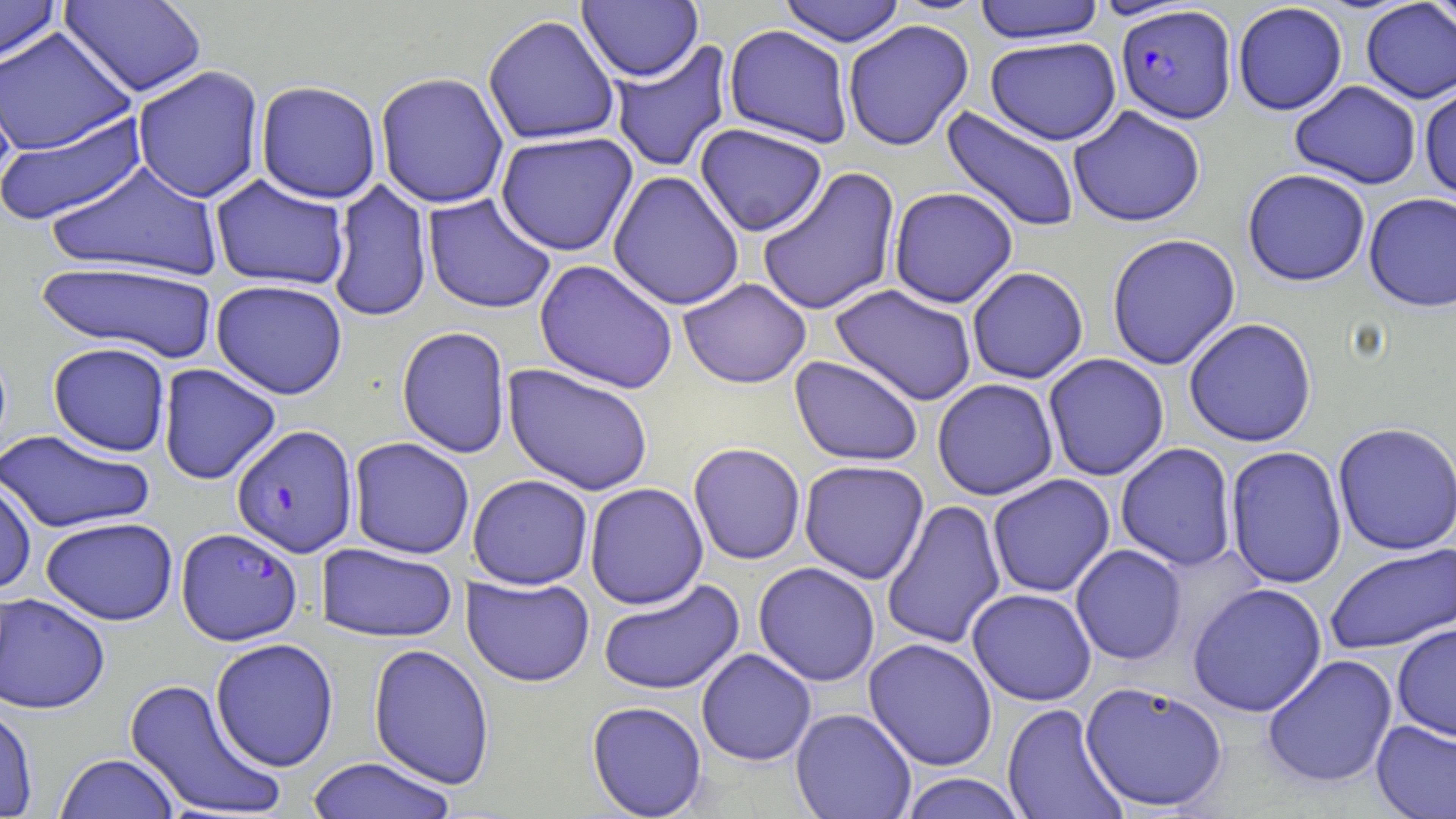

Approximate bounding boxes as (x1,y1)-(x2,y2) corner pairs in pixels. Uninfected red blood cell locations: (0,0)-(63,67), (59,0)-(207,98), (1425,0)-(1455,34), (577,1)-(703,82), (779,1)-(906,47), (973,1)-(1107,44), (1232,2)-(1348,116), (1359,2)-(1456,104), (482,13)-(620,146), (842,19)-(973,151), (723,24)-(855,148), (0,26)-(136,156), (985,36)-(1122,145), (609,39)-(734,173), (0,56)-(19,196), (131,65)-(265,203), (374,71)-(510,209), (254,80)-(382,204), (1289,80)-(1422,189), (1418,84)-(1456,201), (1068,105)-(1206,227), (940,106)-(1081,235), (0,110)-(148,226), (694,123)-(828,237), (494,131)-(638,257), (45,160)-(224,282), (757,166)-(901,317), (1242,168)-(1371,287), (607,170)-(745,311), (209,174)-(351,291), (327,179)-(433,323), (888,187)-(1019,308), (1363,192)-(1456,312), (422,194)-(557,315), (1105,233)-(1241,370), (534,259)-(679,394), (35,260)-(220,361), (966,266)-(1089,384), (678,277)-(812,389), (210,279)-(348,399), (830,284)-(978,406), (1183,317)-(1318,447), (396,325)-(512,459), (47,341)-(172,456), (1043,353)-(1170,481), (789,356)-(924,467), (157,364)-(281,485), (502,364)-(654,496), (932,378)-(1058,500), (1332,422)-(1456,555), (0,429)-(155,534), (348,437)-(475,559), (688,442)-(806,565), (1115,442)-(1238,571), (1225,446)-(1347,589), (798,460)-(929,584), (467,474)-(593,590), (987,474)-(1115,598), (0,476)-(37,596), (584,483)-(709,609), (880,499)-(1006,650), (41,516)-(178,626), (316,542)-(458,643), (1324,543)-(1456,654), (1070,544)-(1187,665), (753,562)-(880,686), (461,575)-(595,687), (597,579)-(745,696), (1186,583)-(1327,717), (967,588)-(1097,706), (0,592)-(111,714), (1392,622)-(1456,741), (863,637)-(998,771), (210,638)-(339,772), (368,643)-(496,790), (696,648)-(817,766), (1262,654)-(1398,789), (124,677)-(287,818), (1079,680)-(1228,813), (586,700)-(708,818), (0,703)-(38,819), (1001,703)-(1128,819), (790,708)-(917,819), (1370,719)-(1456,819), (53,753)-(180,818), (305,758)-(458,819), (897,773)-(1029,818). Plasmodium falciparum-infected red blood cell locations: (1116,5)-(1236,124), (231,424)-(359,557), (176,527)-(303,646). Slide-level diagnosis: Plasmodium falciparum. Optical microscopy. Image is 1456×819 pixels. Captured at 1000x magnification. Single field of view. Thin blood film. May-Grünwald-Giemsa-stained preparation.